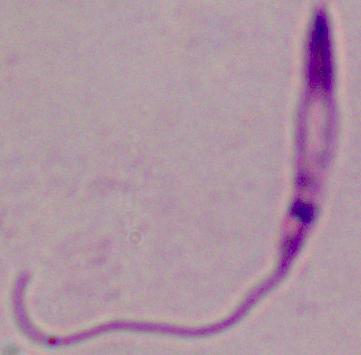
{
  "modality": "micrograph",
  "identification": "Leishmania",
  "magnification": "1000x"
}